Look for Plasmodium parasites.
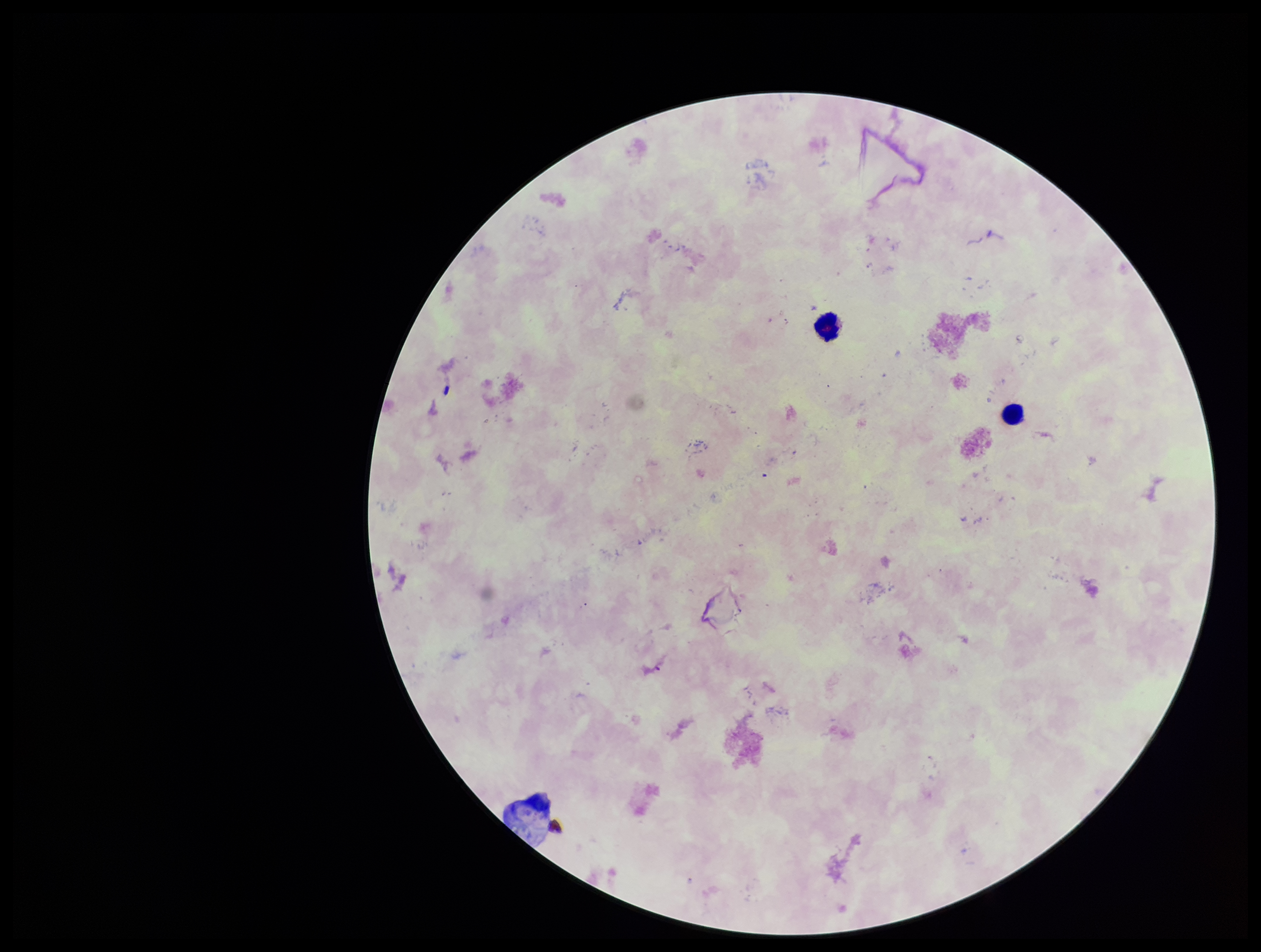
None identified.

Photographed through the microscope eyepiece with a smartphone camera. Single field of view. Leukocyte count: 2. Image is 1261×952 pixels. Stained with Giemsa. Patient malaria status: negative. Preparation: thick. Parasite count: 0.